Point out each Plasmodium parasite.
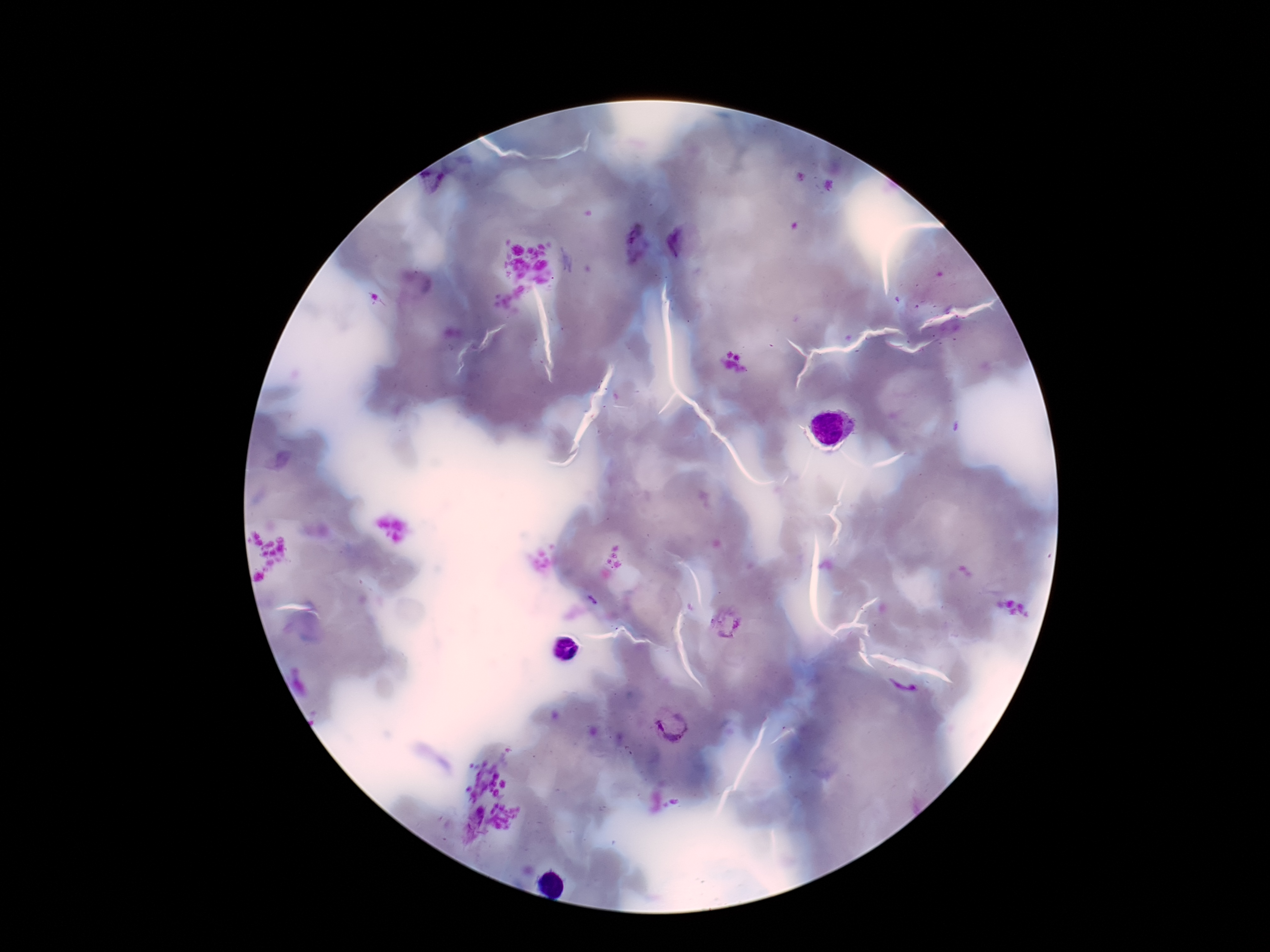
Approximate centers as [x, y] in pixels.
Plasmodium parasites: [432, 182], [632, 241], [682, 241], [592, 600], [727, 623], [903, 686], [673, 728].

Summary:
  - Stain: Giemsa
  - Magnification: 100x
  - Field of view: one from this slide
  - Capture: smartphone camera through the microscope eyepiece
  - Patient malaria status: infected
  - Image size: 1270×952 pixels
  - Preparation: thick peripheral-blood smear